Name the parasite shown.
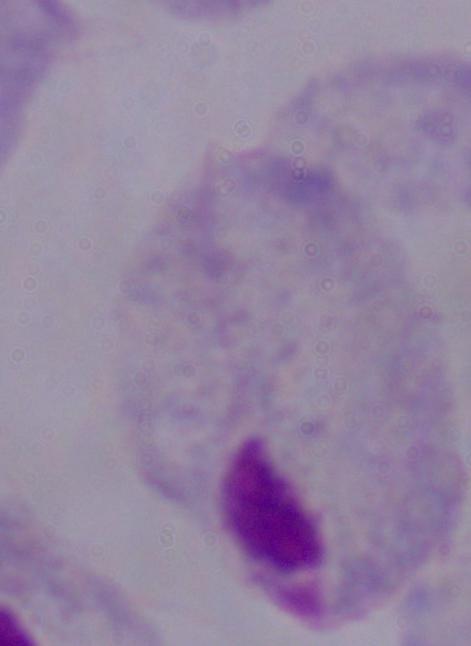

This is a trichomonad.

Summary:
  - Magnification: 1000x
  - Modality: micrograph